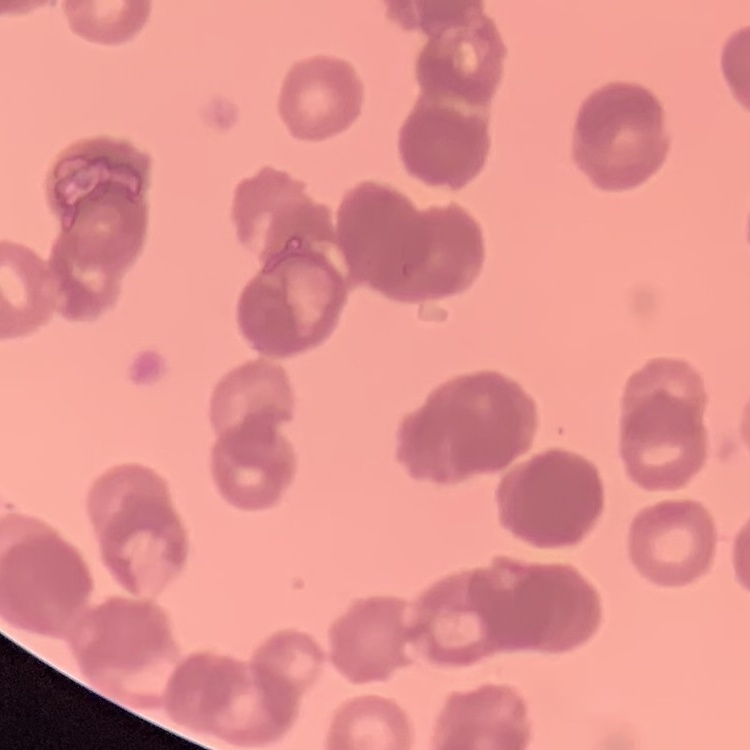
Summary:
  - Red blood cell morphology: rouleaux formation
  - Preparation: thin peripheral smear
  - Image type: square crop of a larger photomicrograph
  - Stain: Field's or Giemsa